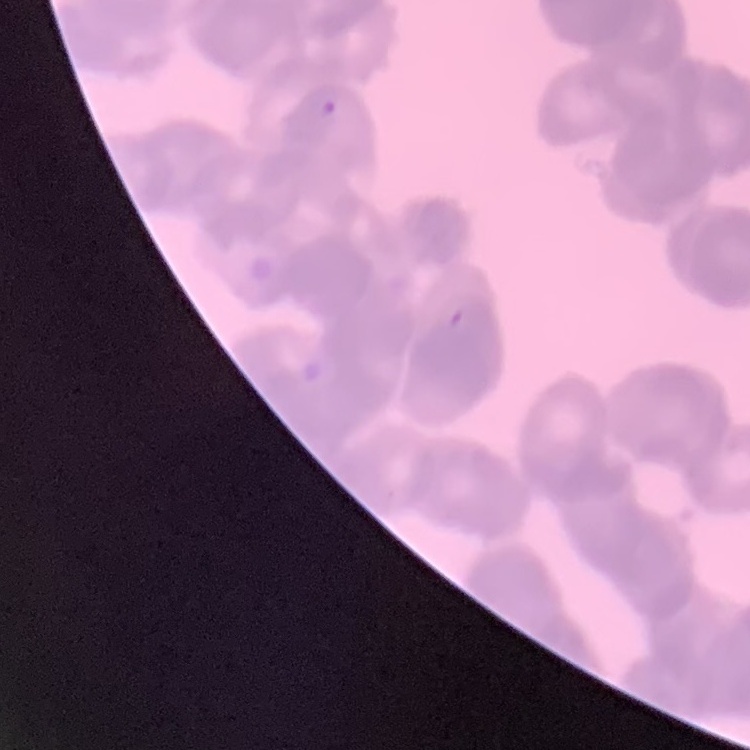
Summary:
  - Red blood cell morphology: rouleaux formation
  - Preparation: thin peripheral smear
  - Image type: square crop of a larger photomicrograph
  - Stain: Field's or Giemsa